Assess this cell for malaria.
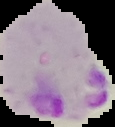
Parasitized.

Image is 115×127 pixels. The area outside the segmented cell region is set to black. From a thin blood smear.